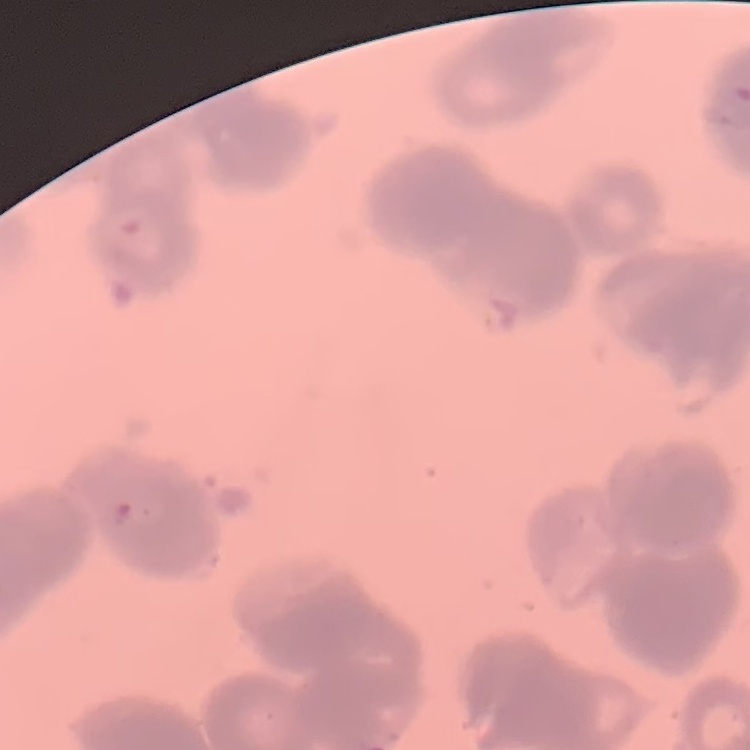
The red blood cells show rouleaux formation. Thin peripheral smear. Stained with either Field's or Giemsa. Square crop of a larger photomicrograph.